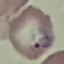 Result: malaria parasites detected. Giemsa-stained preparation. Thin blood smear. Cell patch, automatically extracted from a larger field of view and resized to 64 × 64 pixels. Photographed with a smartphone camera at the microscope eyepiece.